Point out each Plasmodium parasite.
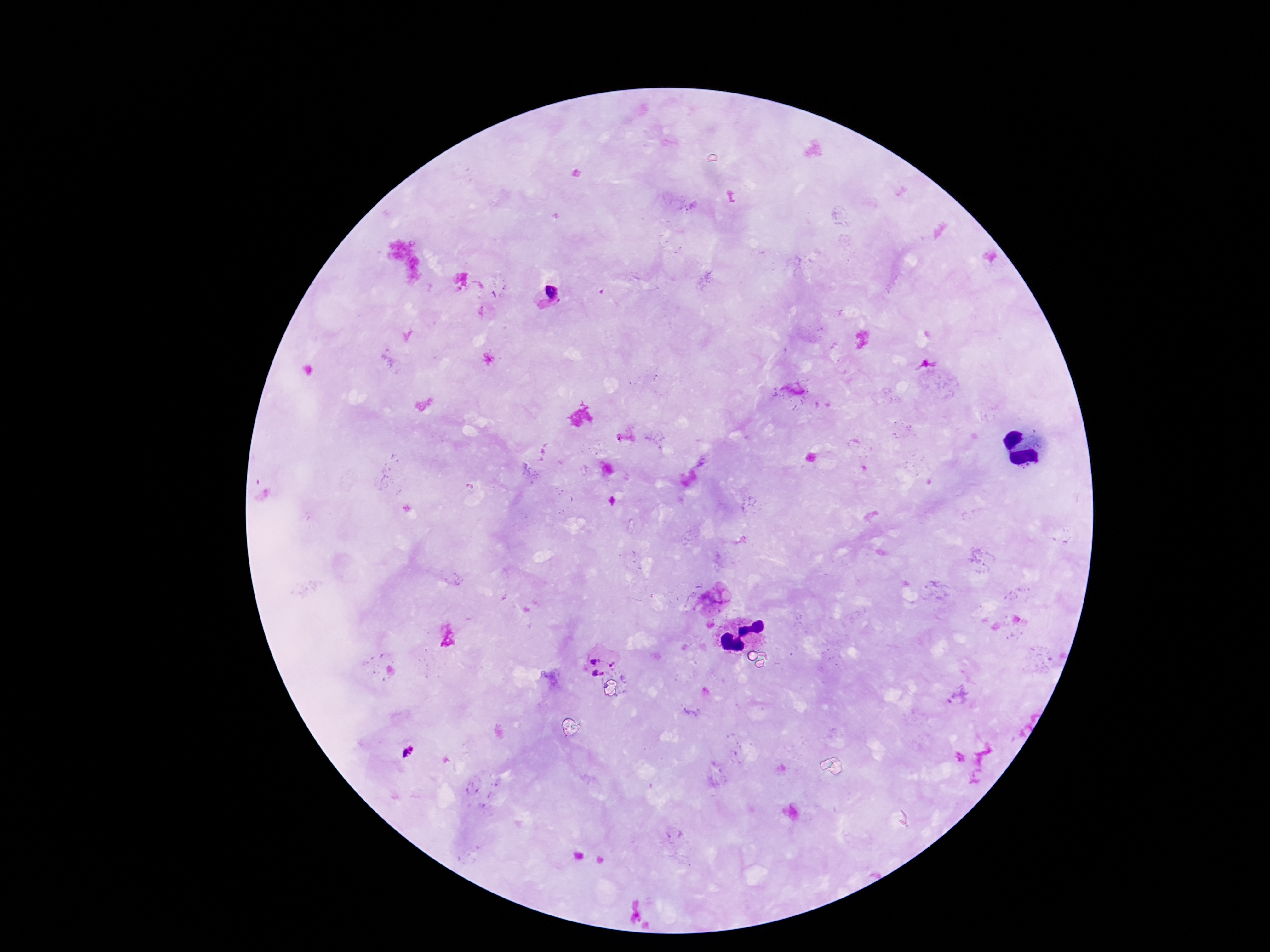

Approximate centers as {x, y} in pixels.
Plasmodium parasites: {552, 289}, {716, 597}, {595, 660}, {613, 664}, {597, 673}.

Summary:
  - Stain: Giemsa
  - Capture: smartphone camera through the microscope eyepiece
  - Field of view: single
  - Magnification: 100x
  - Preparation: thick blood film
  - Patient malaria status: infected
  - Image size: 1270×952 pixels